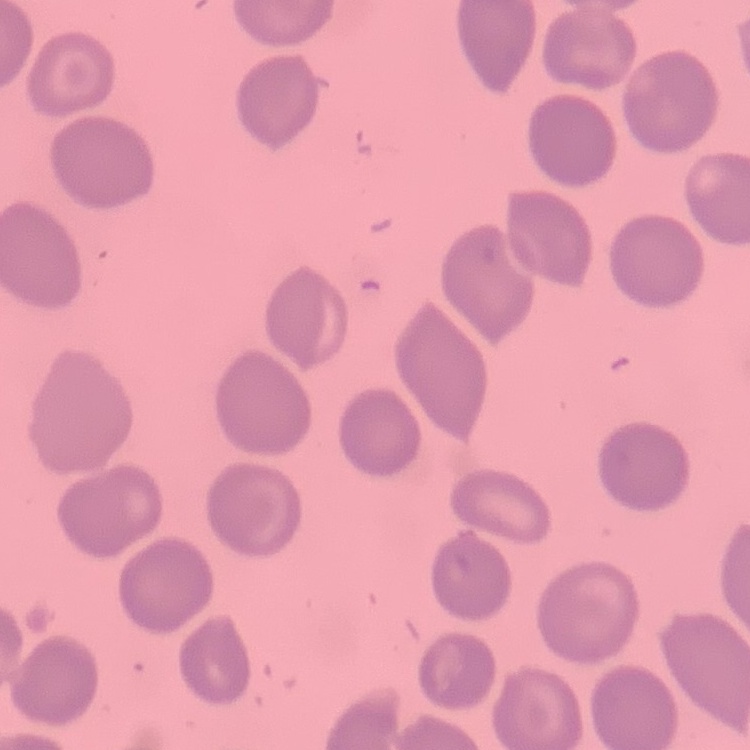 The erythrocytes show no rouleaux formation. Square crop of a larger photomicrograph. Thin blood film. Stained with either Field's or Giemsa.